Name the parasite shown.
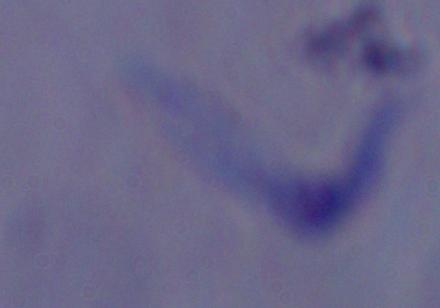
A trypanosome.

Summary:
  - Modality: micrograph
  - Magnification: 1000x